Comment on the morphology of the red blood cells.
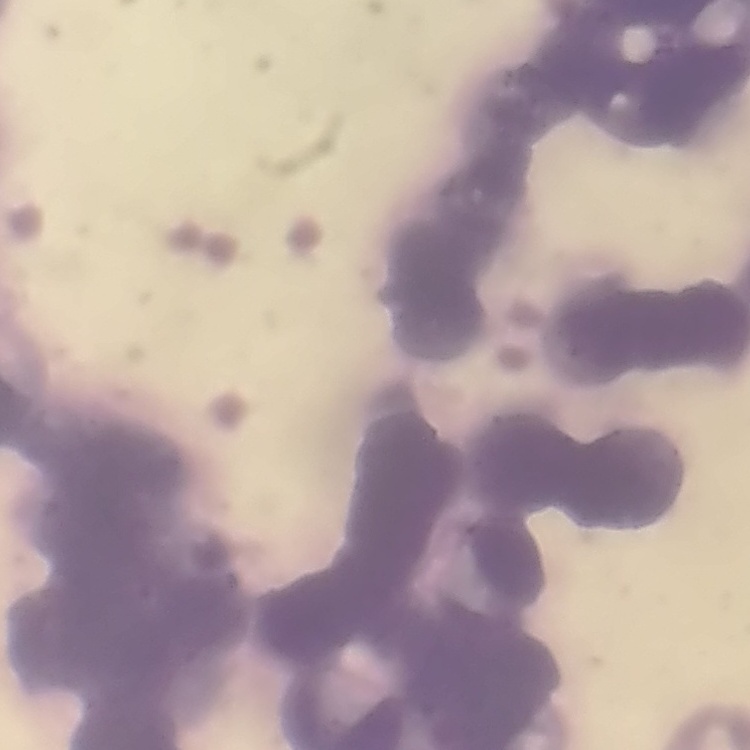

They show rouleaux formation.

stain: Field's or Giemsa
image_type: one tile cut from a larger photomicrograph
preparation: thin blood smear